Identify the parasite.
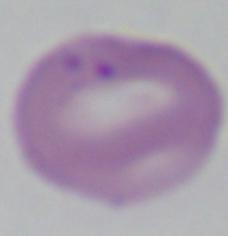
This is Babesia.

Summary:
  - Magnification: 1000x
  - Modality: photomicrograph